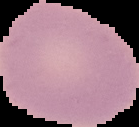
{
  "preparation": "thin blood smear",
  "image_size": "139×127 pixels",
  "malaria_status": "uninfected",
  "image_type": "segmented cell region on a black background"
}